State which cell type is depicted.
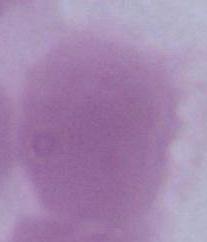

An erythrocyte.

Summary:
  - Modality: micrograph
  - Magnification: 1000x